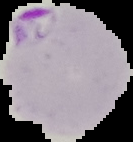 From a thin blood film. Image is 133×142 pixels. Result: Plasmodium parasites detected. The area outside the segmented cell region is set to black.